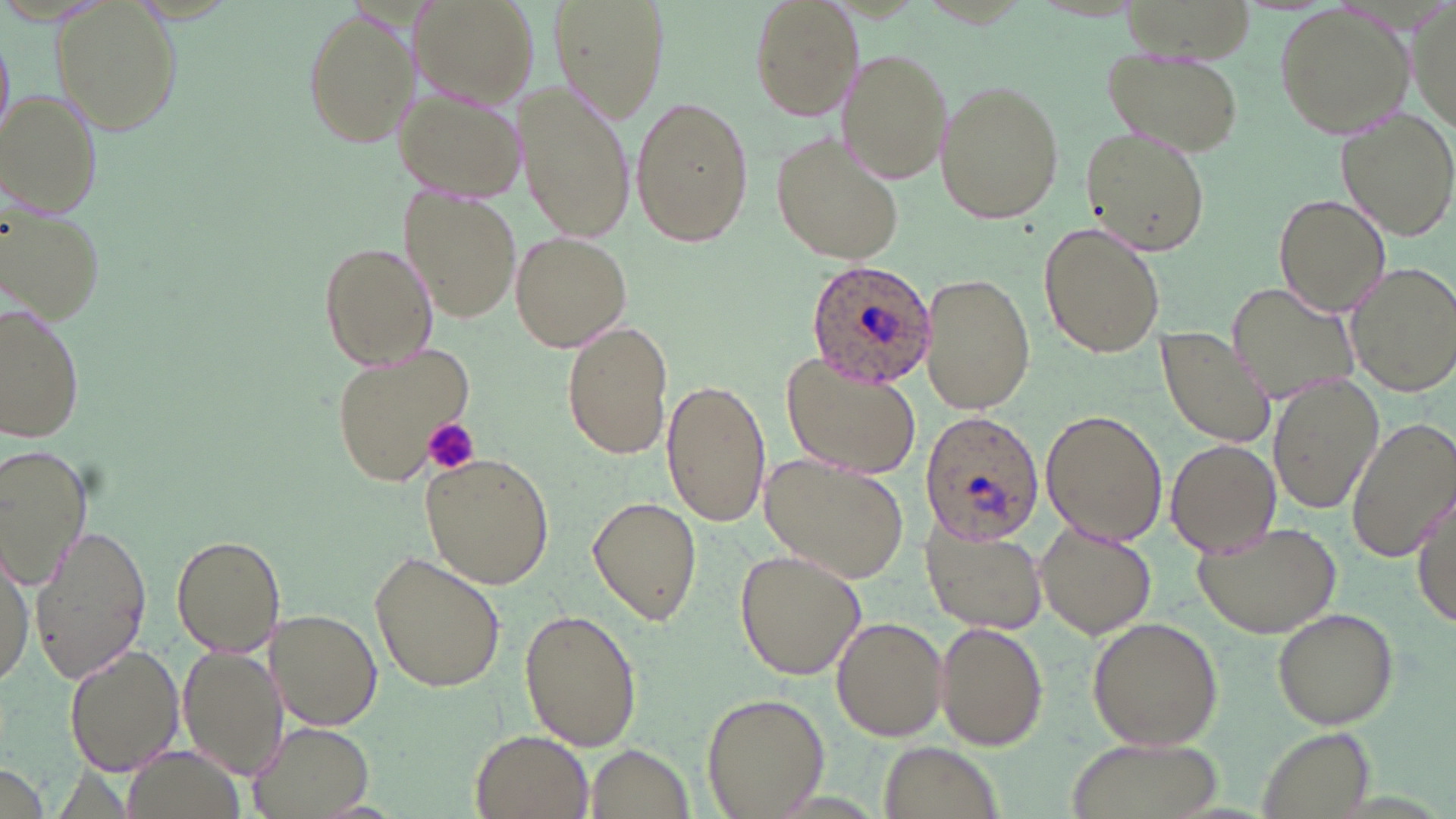

slide_level_diagnosis: Plasmodium ovale
platelet_locations: 'approximate bounding boxes as named x1/y1/x2/y2 corners in pixels: (x1=423, y1=417, x2=479, y2=476)'
magnification: 1000x
preparation: thin blood film
field_of_view: single
image_size: 1456×819 pixels
modality: light microscopy
uninfected_red_blood_cell_locations: 'approximate bounding boxes as named x1/y1/x2/y2 corners in pixels: (x1=413, y1=0, x2=541, y2=111), (x1=551, y1=0, x2=669, y2=125), (x1=745, y1=0, x2=863, y2=118), (x1=1409, y1=0, x2=1455, y2=138), (x1=51, y1=3, x2=184, y2=138), (x1=1273, y1=4, x2=1414, y2=140), (x1=299, y1=9, x2=418, y2=149), (x1=0, y1=34, x2=14, y2=145), (x1=1102, y1=45, x2=1245, y2=159), (x1=838, y1=48, x2=952, y2=185), (x1=936, y1=80, x2=1063, y2=224), (x1=514, y1=82, x2=638, y2=243), (x1=394, y1=85, x2=528, y2=203), (x1=0, y1=88, x2=102, y2=219), (x1=631, y1=95, x2=753, y2=247), (x1=1335, y1=108, x2=1456, y2=242), (x1=1084, y1=126, x2=1209, y2=256), (x1=775, y1=135, x2=906, y2=263), (x1=2, y1=191, x2=109, y2=324), (x1=403, y1=191, x2=521, y2=321), (x1=1272, y1=193, x2=1391, y2=318), (x1=1037, y1=223, x2=1166, y2=359), (x1=509, y1=230, x2=633, y2=353), (x1=317, y1=242, x2=438, y2=371), (x1=1343, y1=261, x2=1456, y2=399), (x1=918, y1=272, x2=1034, y2=416), (x1=1228, y1=283, x2=1365, y2=404), (x1=0, y1=301, x2=86, y2=443), (x1=562, y1=319, x2=675, y2=461), (x1=1155, y1=324, x2=1280, y2=449), (x1=329, y1=344, x2=478, y2=487), (x1=781, y1=352, x2=923, y2=476), (x1=1269, y1=374, x2=1385, y2=514), (x1=660, y1=377, x2=772, y2=526), (x1=1039, y1=408, x2=1168, y2=546), (x1=1347, y1=415, x2=1456, y2=564), (x1=1165, y1=438, x2=1281, y2=556), (x1=0, y1=442, x2=94, y2=590), (x1=419, y1=453, x2=554, y2=589), (x1=757, y1=457, x2=909, y2=584), (x1=1412, y1=490, x2=1455, y2=628), (x1=588, y1=495, x2=702, y2=626), (x1=1190, y1=520, x2=1342, y2=637), (x1=28, y1=523, x2=152, y2=685), (x1=922, y1=523, x2=1047, y2=636), (x1=1036, y1=523, x2=1156, y2=639), (x1=170, y1=532, x2=287, y2=658), (x1=0, y1=548, x2=34, y2=686), (x1=736, y1=549, x2=866, y2=681), (x1=370, y1=550, x2=506, y2=694), (x1=519, y1=606, x2=641, y2=751), (x1=1273, y1=607, x2=1399, y2=728), (x1=265, y1=608, x2=382, y2=730), (x1=1086, y1=615, x2=1224, y2=751), (x1=831, y1=616, x2=950, y2=741), (x1=934, y1=621, x2=1048, y2=751), (x1=63, y1=641, x2=183, y2=777), (x1=176, y1=647, x2=285, y2=780), (x1=701, y1=691, x2=830, y2=817), (x1=247, y1=720, x2=377, y2=819), (x1=1255, y1=725, x2=1377, y2=819), (x1=471, y1=731, x2=592, y2=817), (x1=1064, y1=735, x2=1220, y2=819), (x1=879, y1=738, x2=1000, y2=818), (x1=583, y1=743, x2=698, y2=818), (x1=119, y1=745, x2=247, y2=819), (x1=0, y1=763, x2=49, y2=819)'
plasmodium_ovale_infected_red_blood_cell_locations: 'approximate bounding boxes as named x1/y1/x2/y2 corners in pixels: (x1=804, y1=259, x2=938, y2=389), (x1=917, y1=412, x2=1042, y2=548)'
stain: May-Grünwald-Giemsa